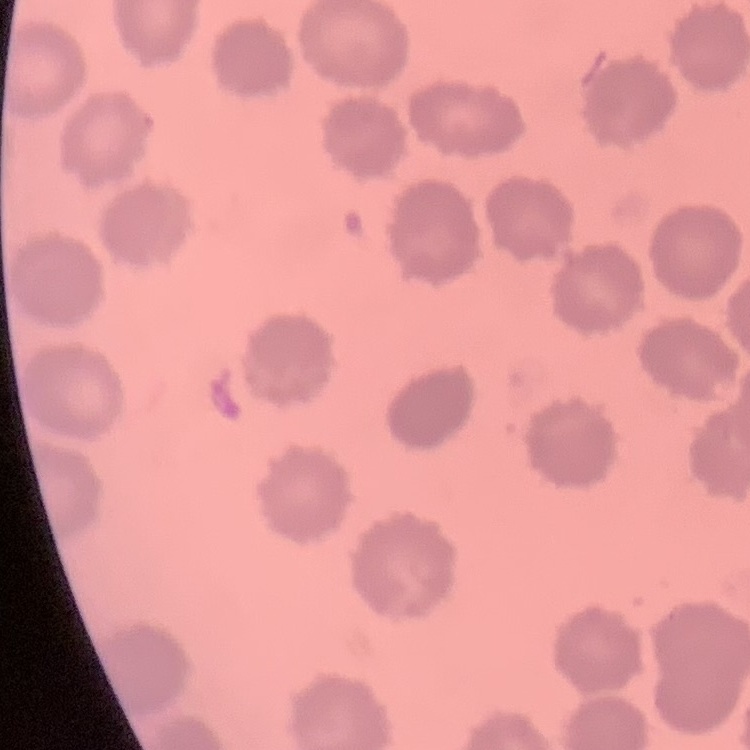

{
  "erythrocyte_morphology": "no rouleaux formation",
  "preparation": "thin peripheral smear",
  "stain": "Field's or Giemsa",
  "image_type": "one tile cut from a larger photomicrograph"
}